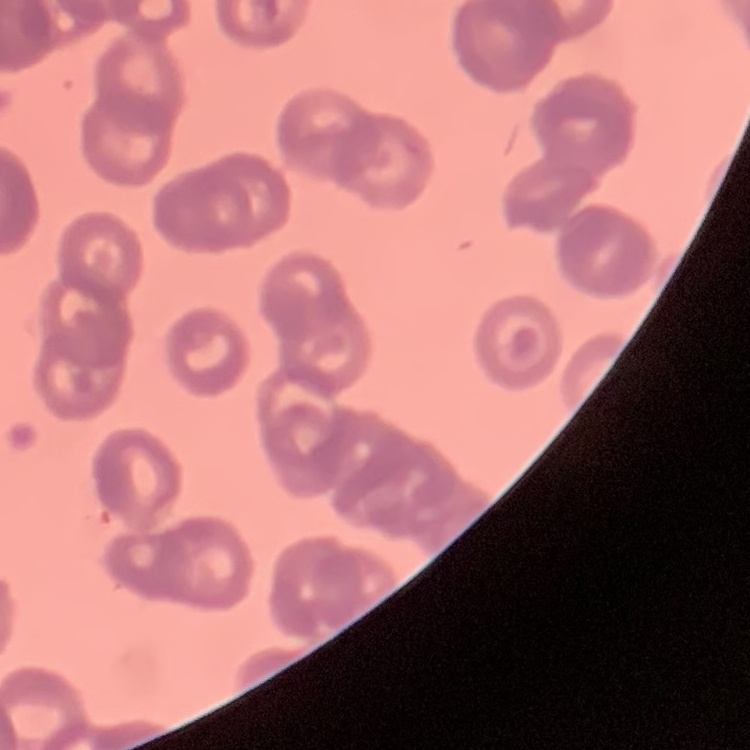
Summary:
  - Erythrocyte morphology: rouleaux formation
  - Stain: Field's or Giemsa
  - Preparation: thin peripheral smear
  - Image type: square crop of a larger photomicrograph